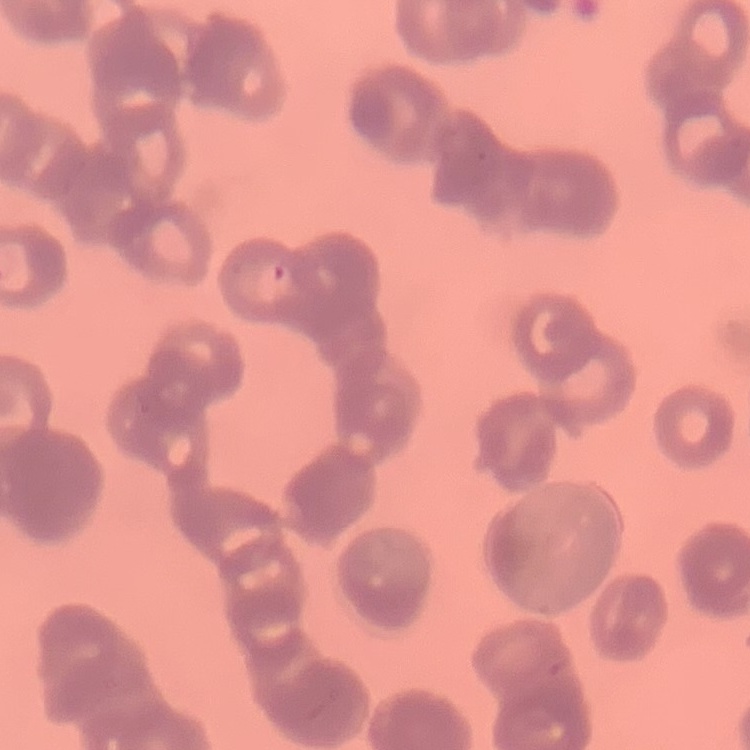 The erythrocytes show rouleaux formation. One tile cut from a larger photomicrograph. Field's or Giemsa stain. Thin blood smear.